Report the malaria status of this cell.
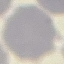

Uninfected.

stain = Giemsa
preparation = thin smear
capture = smartphone camera at the microscope eyepiece
image type = automatically extracted cell patch, resized to 64 × 64 pixels